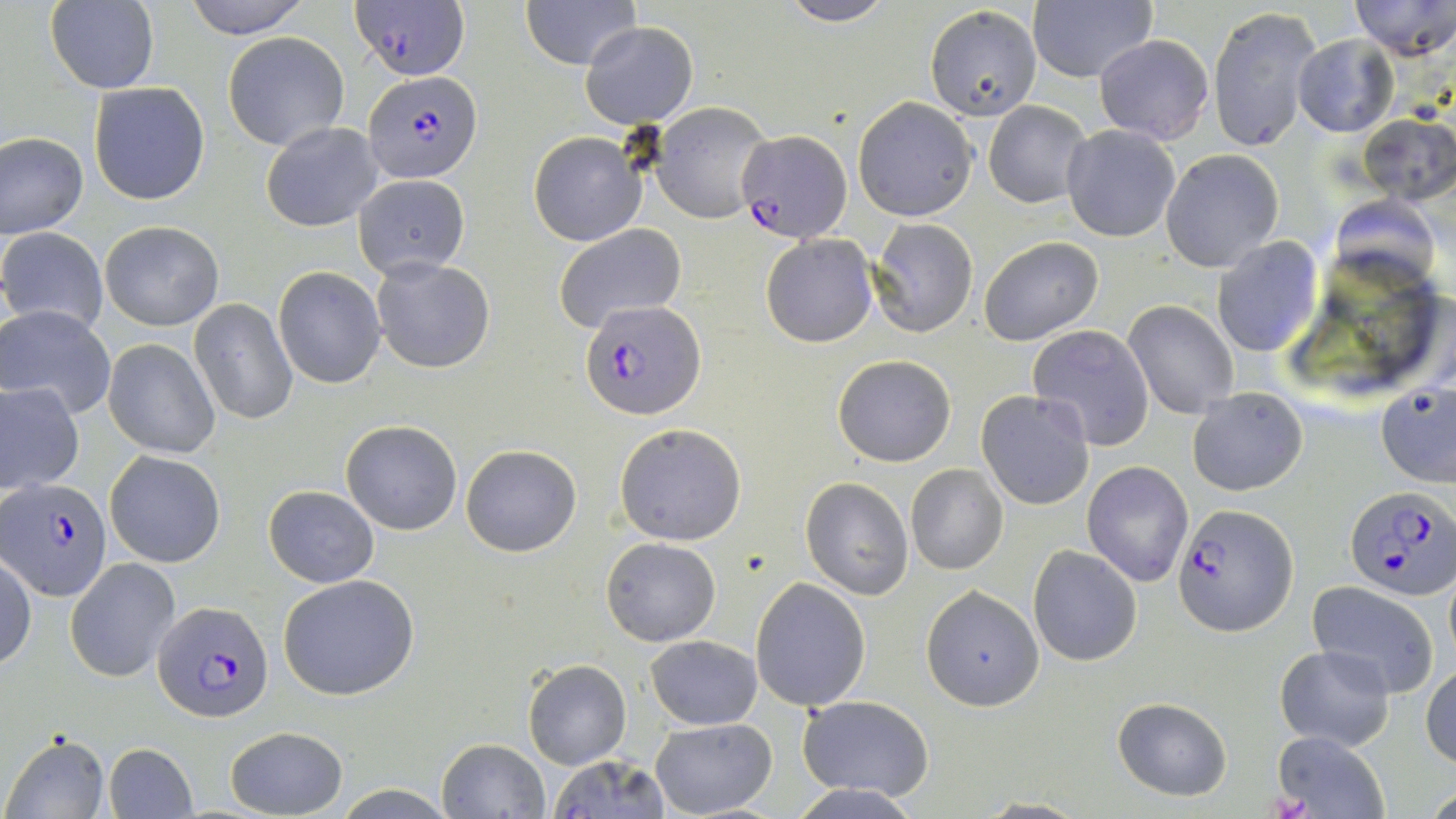
Summary:
  - Coordinate format: approximate bounding boxes as [x1, y1, x2, y2] in pixels
  - Plasmodium falciparum-infected red blood cell locations: [354, 0, 470, 80], [364, 71, 479, 180], [737, 129, 850, 239], [581, 300, 705, 421], [4, 479, 113, 602], [1345, 487, 1455, 600], [1176, 504, 1298, 634], [154, 599, 274, 721]
  - Uninfected red blood cell locations: [183, 0, 311, 36], [519, 0, 642, 69], [778, 0, 898, 26], [1028, 0, 1156, 84], [1350, 0, 1455, 59], [47, 1, 159, 94], [924, 5, 1041, 120], [1208, 5, 1324, 155], [580, 21, 699, 128], [222, 31, 350, 151], [1094, 34, 1215, 145], [1292, 34, 1398, 138], [88, 81, 212, 206], [853, 97, 977, 222], [651, 101, 773, 222], [983, 101, 1091, 207], [1357, 112, 1455, 205], [260, 122, 383, 232], [1062, 125, 1179, 242], [527, 131, 646, 246], [1, 132, 88, 237], [1161, 149, 1284, 273], [352, 175, 471, 278], [868, 218, 978, 338], [99, 219, 223, 331], [553, 222, 689, 333], [0, 228, 109, 336], [761, 234, 879, 348], [1212, 236, 1323, 359], [978, 237, 1104, 346], [370, 256, 496, 374], [273, 267, 388, 389], [189, 299, 298, 425], [1124, 301, 1239, 421], [1, 306, 116, 420], [1027, 325, 1156, 451], [104, 338, 221, 459], [831, 354, 956, 466], [1376, 379, 1455, 489], [0, 381, 85, 495], [1187, 387, 1308, 496], [976, 389, 1095, 510], [341, 420, 463, 536], [614, 422, 747, 545], [459, 444, 582, 557], [105, 452, 225, 567], [1083, 461, 1193, 586], [904, 464, 1008, 576], [800, 477, 914, 600], [263, 485, 381, 588], [600, 537, 721, 647], [1029, 545, 1143, 665], [1, 555, 36, 671], [64, 558, 181, 683], [279, 573, 422, 700], [750, 579, 870, 709], [1306, 580, 1440, 698], [921, 586, 1043, 710], [646, 635, 762, 730], [1274, 645, 1396, 750], [522, 659, 631, 769], [1421, 661, 1456, 768], [796, 694, 936, 801], [1111, 696, 1233, 801], [650, 718, 777, 818], [223, 726, 347, 818], [1273, 731, 1388, 816], [4, 732, 109, 818], [437, 738, 549, 818], [102, 742, 197, 819], [547, 755, 669, 818], [786, 783, 925, 818], [971, 797, 1088, 817]
  - Slide-level diagnosis: Plasmodium falciparum
  - Preparation: thin blood film
  - Image size: 1456×819 pixels
  - Magnification: 1000x
  - Stain: May-Grünwald-Giemsa
  - Field of view: one of a larger specimen
  - Modality: optical microscopy